Comment on the morphology of the red blood cells.
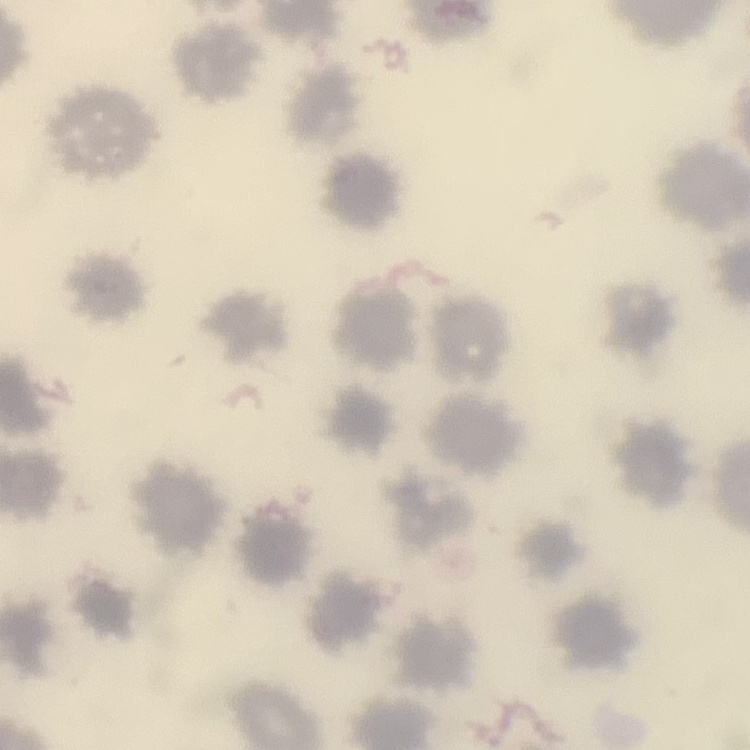

No rouleaux formation.

stain = Field's or Giemsa
image type = one tile cut from a larger photomicrograph
preparation = thin blood film